Name the parasite shown.
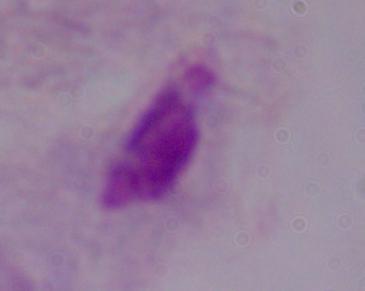

This is a trichomonad.

Photomicrograph. Captured at 1000x magnification.